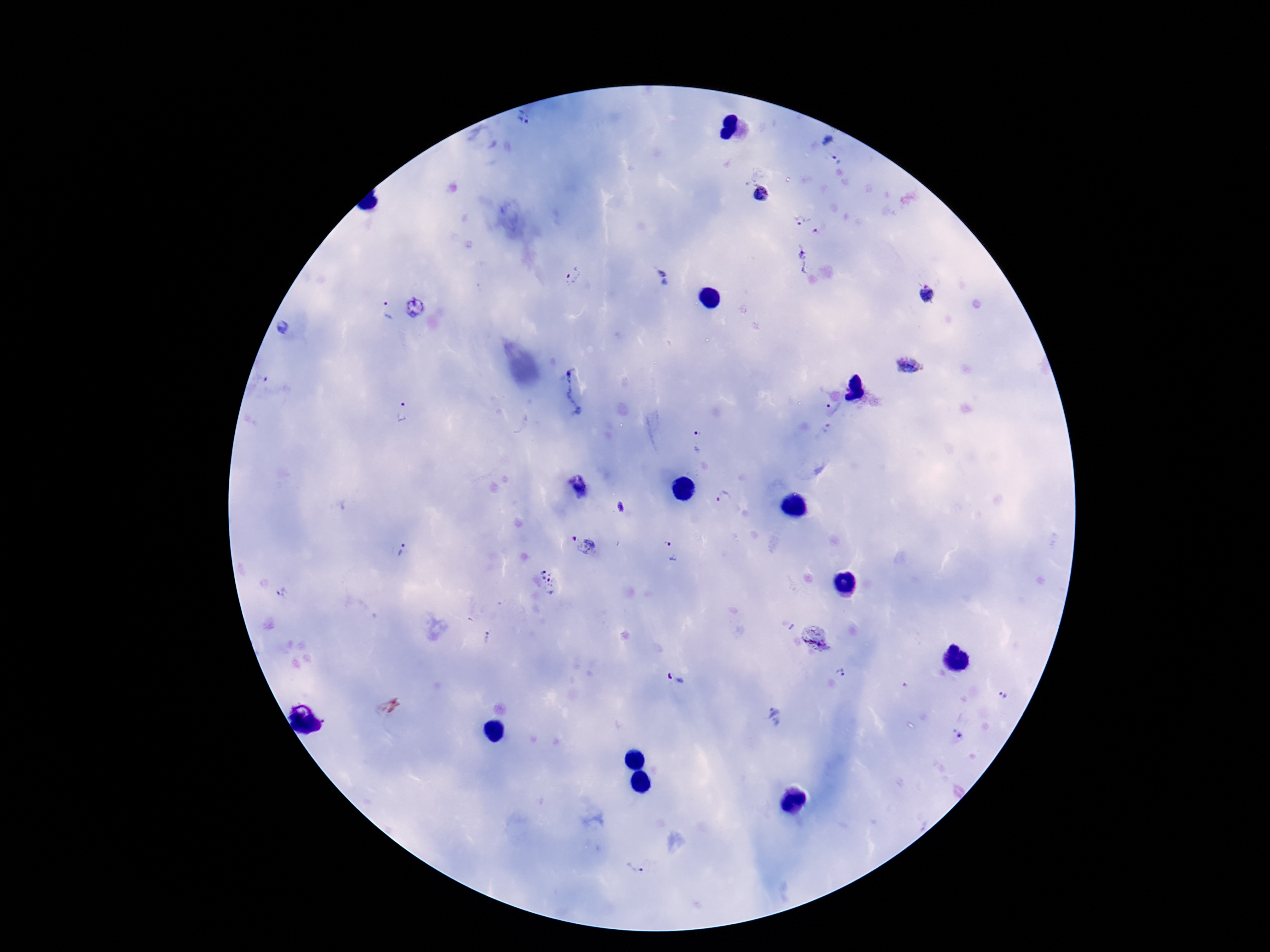

Approximate object centers, in pixels from the top-left corner.
Summary:
  - Plasmodium parasite locations: (x=525, y=122), (x=828, y=139), (x=835, y=159), (x=762, y=193), (x=800, y=220), (x=817, y=229), (x=802, y=259), (x=660, y=272), (x=573, y=275), (x=666, y=284), (x=925, y=293), (x=387, y=309), (x=283, y=327), (x=912, y=364), (x=260, y=378), (x=573, y=394), (x=833, y=409), (x=400, y=411), (x=698, y=441), (x=579, y=487), (x=723, y=498), (x=621, y=506), (x=573, y=537), (x=587, y=546), (x=402, y=550), (x=671, y=552), (x=546, y=582), (x=282, y=594), (x=486, y=637), (x=814, y=638), (x=842, y=672), (x=675, y=679), (x=1003, y=695), (x=774, y=718), (x=957, y=736), (x=636, y=868)
  - Magnification: 100x
  - Patient malaria status: positive
  - Field of view: single
  - Image size: 1270×952 pixels
  - Capture: smartphone camera through the microscope eyepiece
  - Stain: Giemsa
  - Preparation: thick blood film